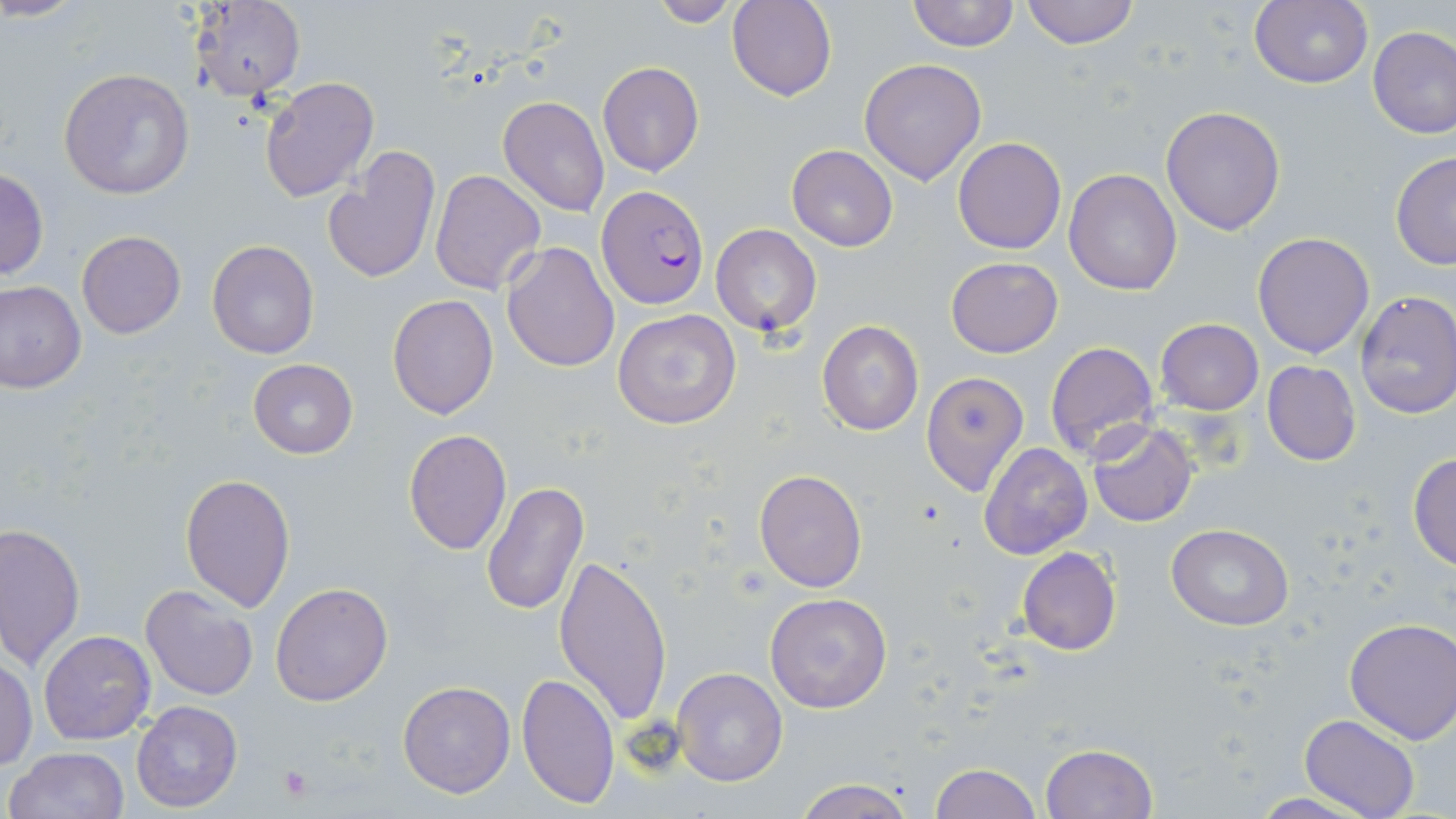

Approximate bounding boxes as (x1, y1, x2, y2) in pixels. Platelet locations: (277, 766, 312, 800). Uninfected red blood cell locations: (727, 0, 837, 100), (906, 0, 1020, 51), (1021, 0, 1139, 49), (188, 1, 306, 104), (646, 1, 747, 26), (1247, 1, 1376, 87), (1367, 26, 1456, 139), (859, 58, 987, 185), (597, 62, 705, 178), (58, 67, 194, 199), (260, 77, 380, 203), (498, 96, 610, 218), (1160, 106, 1286, 236), (954, 137, 1067, 255), (787, 143, 898, 252), (323, 145, 442, 287), (1389, 152, 1456, 270), (0, 166, 49, 282), (431, 169, 546, 294), (1064, 169, 1182, 296), (711, 224, 822, 336), (76, 230, 185, 339), (1252, 232, 1376, 358), (206, 239, 320, 361), (501, 241, 619, 372), (946, 257, 1063, 357), (1, 280, 86, 392), (1354, 290, 1456, 419), (387, 294, 498, 420), (613, 308, 742, 430), (817, 319, 924, 436), (1156, 319, 1264, 414), (1044, 341, 1159, 461), (247, 359, 358, 458), (1262, 361, 1361, 467), (920, 370, 1032, 497), (1086, 421, 1198, 528), (403, 428, 512, 555), (979, 441, 1093, 560), (1409, 452, 1456, 571), (753, 467, 867, 593), (180, 474, 296, 614), (482, 482, 588, 615), (0, 522, 85, 670), (1167, 524, 1294, 630), (1017, 548, 1121, 656), (553, 549, 673, 727), (270, 581, 393, 706), (140, 584, 259, 702), (765, 593, 893, 711), (1344, 617, 1456, 745), (39, 631, 156, 745), (1, 658, 37, 770), (673, 667, 788, 786), (517, 672, 620, 807), (398, 681, 515, 798), (131, 700, 241, 813), (1300, 714, 1420, 819), (1039, 742, 1159, 818), (6, 747, 131, 819), (930, 763, 1041, 818), (794, 778, 915, 819), (1242, 792, 1378, 819). Plasmodium falciparum-infected red blood cell locations: (596, 184, 710, 307). Slide-level diagnosis: Plasmodium falciparum. Image is 1456×819 pixels. Optical microscopy. May-Grünwald-Giemsa stain. Captured at 1000x magnification. Thin blood smear. Single field of view.